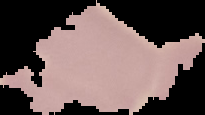
{
  "malaria_status": "uninfected",
  "preparation": "thin blood smear",
  "image_type": "segmented cell region on a black background",
  "image_size": "205×115 pixels"
}